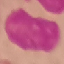

result = negative for malaria parasites
stain = Giemsa
capture = smartphone through the microscope eyepiece
image type = automatically extracted cell patch, resized to 64 × 64 pixels
preparation = thin blood film